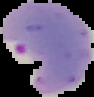

{
  "image_type": "segmented cell region with the area outside set to black",
  "image_size": "94×97 pixels",
  "preparation": "thin blood film",
  "malaria_status": "parasitized"
}